Report the malaria status of this cell.
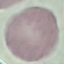

Uninfected.

Automatically extracted cell patch, resized to 64 × 64 pixels. Giemsa stain. Thin blood film. Photographed with a smartphone camera at the microscope eyepiece.